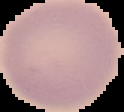 The area outside the segmented cell region is set to black. Image is 124×112 pixels. From a thin blood smear. Result: no malaria parasites seen.